Locate every Plasmodium parasite.
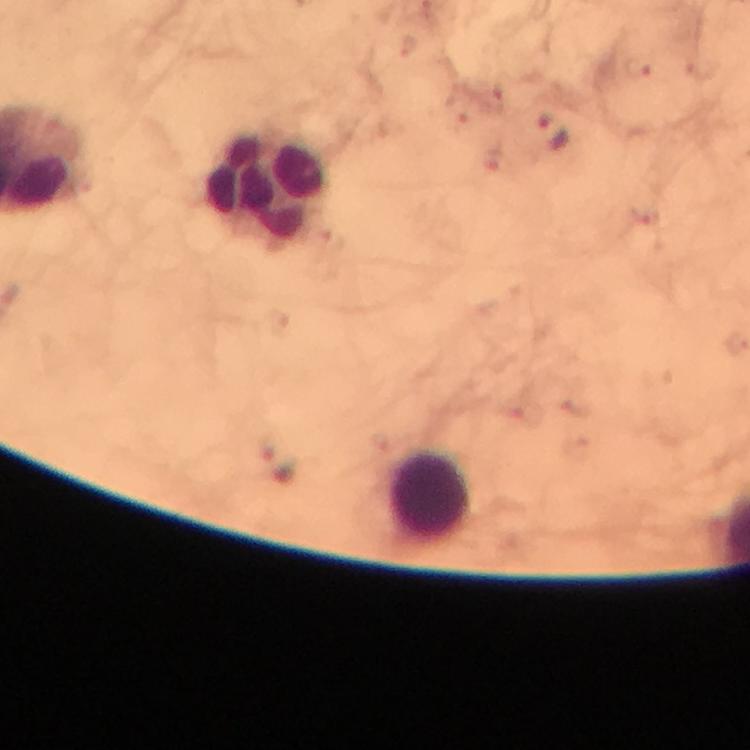
Approximate centers as [x, y] in pixels.
Plasmodium parasites: [639, 70], [554, 132].

Summary:
  - Leukocyte locations: [268, 187], [432, 497]
  - Cropped from: one field of view
  - Preparation: thick blood film
  - Capture: smartphone mounted on the microscope
  - Immersion oil: used
  - Magnification: 100x
  - Context: from a diagnostic examination for malaria
  - Stain: Giemsa
  - Image size: 750×750 pixels